Locate every Plasmodium parasite.
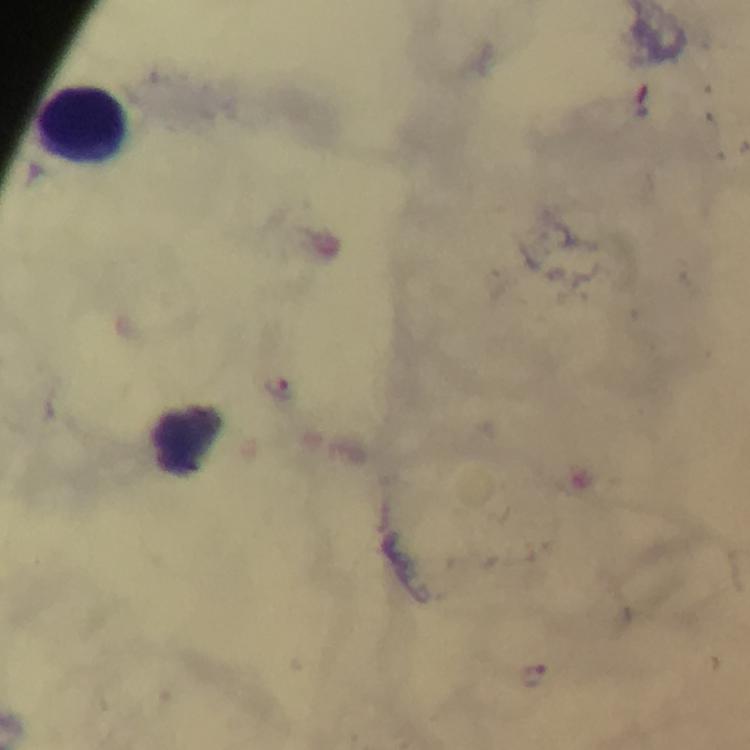

Approximate centers as {x, y} in pixels.
Plasmodium parasites: {278, 387}, {532, 676}.

Summary:
  - Leukocyte locations: {83, 123}
  - Image size: 750×750 pixels
  - Magnification: 100x
  - Capture: smartphone photograph through a microscope
  - Cropped from: one field of view
  - Immersion oil: applied
  - Preparation: thick blood film
  - Context: from a diagnostic examination for malaria
  - Stain: Giemsa